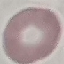
Summary:
  - Malaria status: uninfected
  - Stain: Giemsa
  - Capture: smartphone camera at the microscope eyepiece
  - Image type: cell patch, automatically extracted from a larger field of view and resized to 64 × 64 pixels
  - Preparation: thin blood film